Name the blood parasite species.
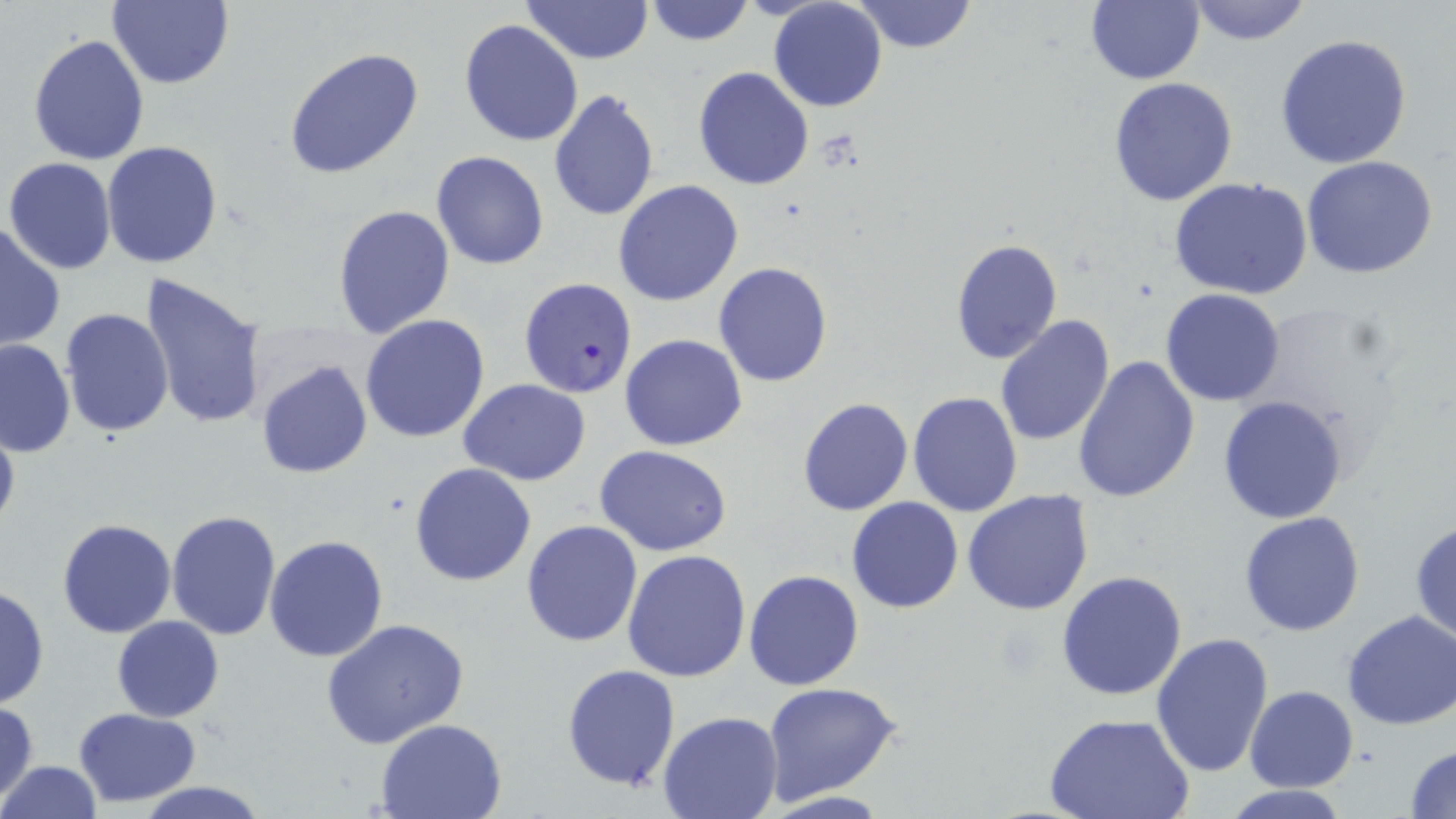

Plasmodium falciparum.

Summary:
  - Coordinate format: approximate bounding boxes as [x1, y1, x2, y2] in pixels
  - Uninfected red blood cell locations: [108, 0, 233, 89], [523, 0, 653, 65], [768, 0, 887, 112], [854, 0, 977, 54], [1186, 0, 1313, 46], [643, 1, 756, 48], [1085, 1, 1205, 85], [459, 20, 584, 148], [1274, 33, 1413, 170], [28, 34, 150, 166], [283, 47, 426, 180], [693, 66, 814, 191], [1108, 78, 1239, 206], [548, 88, 659, 222], [101, 140, 224, 268], [431, 150, 550, 271], [1300, 156, 1438, 280], [3, 157, 118, 273], [1169, 177, 1315, 301], [613, 180, 743, 306], [331, 204, 455, 337], [0, 224, 66, 353], [950, 236, 1063, 364], [713, 262, 833, 386], [139, 272, 267, 432], [1160, 288, 1287, 406], [59, 307, 176, 439], [993, 314, 1115, 448], [360, 315, 490, 443], [619, 334, 748, 452], [0, 339, 75, 455], [1073, 356, 1201, 504], [255, 360, 374, 479], [459, 380, 589, 485], [907, 391, 1025, 517], [1216, 395, 1349, 523], [796, 396, 914, 516], [0, 417, 20, 540], [594, 445, 734, 557], [409, 462, 538, 586], [962, 489, 1095, 614], [846, 496, 963, 614], [166, 510, 281, 642], [1239, 512, 1366, 636], [1409, 518, 1456, 646], [57, 519, 177, 638], [520, 519, 643, 648], [263, 534, 389, 663], [622, 550, 752, 683], [744, 569, 864, 690], [1056, 570, 1189, 702], [0, 585, 48, 709], [1341, 610, 1456, 731], [111, 616, 224, 721], [322, 619, 468, 750], [1150, 633, 1275, 779], [561, 662, 680, 791], [763, 681, 904, 804], [1246, 685, 1358, 792], [1, 702, 39, 801], [73, 708, 202, 807], [657, 712, 782, 819], [1046, 713, 1193, 819], [375, 718, 508, 819], [0, 726, 69, 816], [1406, 743, 1456, 817], [1, 760, 101, 819], [131, 781, 271, 818], [1221, 785, 1354, 818]
  - Plasmodium falciparum-infected red blood cell locations: [518, 278, 638, 399]
  - Modality: optical microscopy
  - Stain: May-Grünwald-Giemsa
  - Field of view: one of a larger specimen
  - Image size: 1456×819 pixels
  - Magnification: 1000x
  - Preparation: thin blood film